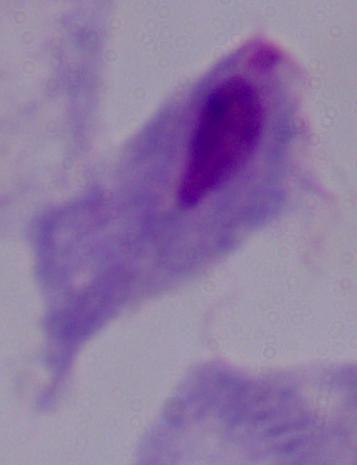 A trichomonad is seen. Photomicrograph. Captured at 1000x magnification.